Assess this cell for malaria.
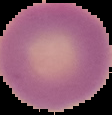
It is uninfected.

From a thin blood smear. Segmented cell region on a black background. Image is 112×115 pixels.